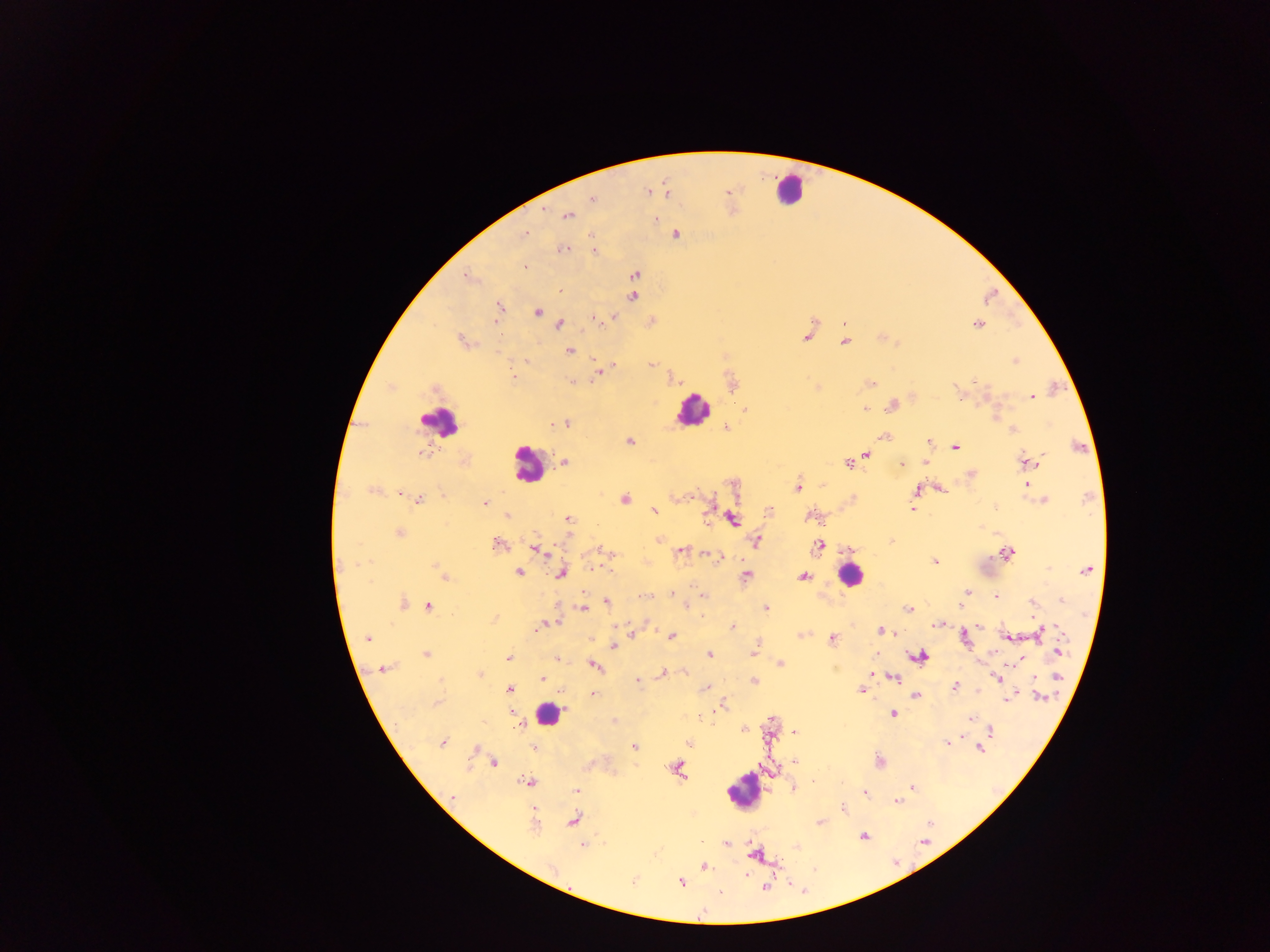
Approximate centers as x y in pixels. Plasmodium parasite locations: 647 192; 726 193; 666 194; 592 198; 566 215; 655 220; 525 234; 675 235; 563 248; 594 251; 524 265; 635 273; 469 276; 559 288; 633 296; 498 306; 536 311; 498 314; 614 316; 595 318; 651 321; 844 323; 559 324; 978 324; 806 334; 882 337; 462 341; 844 341; 569 351; 1014 360; 528 361; 651 363; 611 366; 598 370; 513 378; 671 378; 572 382; 731 383; 869 383; 390 386; 816 387; 435 388; 986 394; 961 395; 1032 395; 912 397; 892 405; 864 408; 744 409; 995 414; 551 423; 565 424; 726 427; 1013 429; 884 437; 629 441; 929 442; 956 447; 1077 447; 421 454; 865 455; 465 461; 564 462; 848 462; 926 462; 1027 462; 901 464; 971 474; 823 484; 734 485; 1025 485; 797 487; 939 487; 374 490; 917 491; 400 493; 852 497; 624 499; 418 500; 1044 500; 484 502; 913 508; 654 511; 769 512; 507 515; 811 516; 566 519; 732 519; 399 532; 659 540; 756 540; 891 541; 496 544; 819 544; 848 549; 537 550; 602 550; 680 551; 707 553; 1007 553; 719 557; 934 561; 593 567; 1087 570; 440 571; 518 572; 560 572; 444 576; 745 576; 804 576; 672 592; 966 592; 645 596; 704 597; 995 597; 1061 600; 606 602; 1032 602; 401 603; 961 605; 428 606; 686 606; 765 607; 583 608; 908 609; 494 618; 554 621; 547 624; 938 624; 540 626; 980 626; 732 627; 535 628; 881 630; 632 632; 1039 633; 671 635; 801 635; 1008 636; 366 637; 963 637; 832 639; 755 646; 613 647; 753 651; 1058 651; 425 653; 708 654; 874 654; 918 656; 508 658; 556 659; 1019 659; 1017 663; 780 664; 593 666; 381 668; 685 672; 663 673; 479 674; 892 676; 1057 677; 542 678; 998 678; 1034 678; 637 679; 754 680; 954 687; 705 688; 508 689; 860 689; 591 693; 561 694; 914 695; 1040 696; 1007 699; 437 703; 723 705; 893 713; 700 717; 970 718; 614 720; 520 725; 743 729; 989 730; 793 732; 946 742; 442 743; 689 743; 533 747; 634 747; 476 748; 979 748; 794 760; 879 761; 493 762; 676 769; 528 782; 911 787; 793 789; 576 790; 863 792; 451 797; 897 801; 844 808; 573 820; 820 822; 534 824; 863 835; 726 843; 582 844; 796 846; 702 866; 681 881; 632 882. Leukocyte locations: 789 189; 693 409; 439 422; 528 464; 849 574; 547 714; 743 791. Thick blood smear. Image is 1270×952 pixels. Mobile-phone photograph taken through the microscope. Sample from Ghana. One field of view.